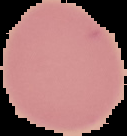
result = no Plasmodium parasites detected
preparation = thin blood film
image type = segmented cell region with the area outside set to black
image size = 127×136 pixels